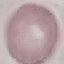
Malaria status: uninfected. Photographed with a smartphone camera at the microscope eyepiece. Giemsa stain. Thin smear of blood. Automatically extracted cell patch, resized to 64 × 64 pixels.